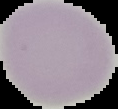

Summary:
  - Image size: 118×109 pixels
  - Image type: segmented cell region with the area outside set to black
  - Preparation: thin blood smear
  - Result: negative for Plasmodium parasites